Outline each Plasmodium parasite.
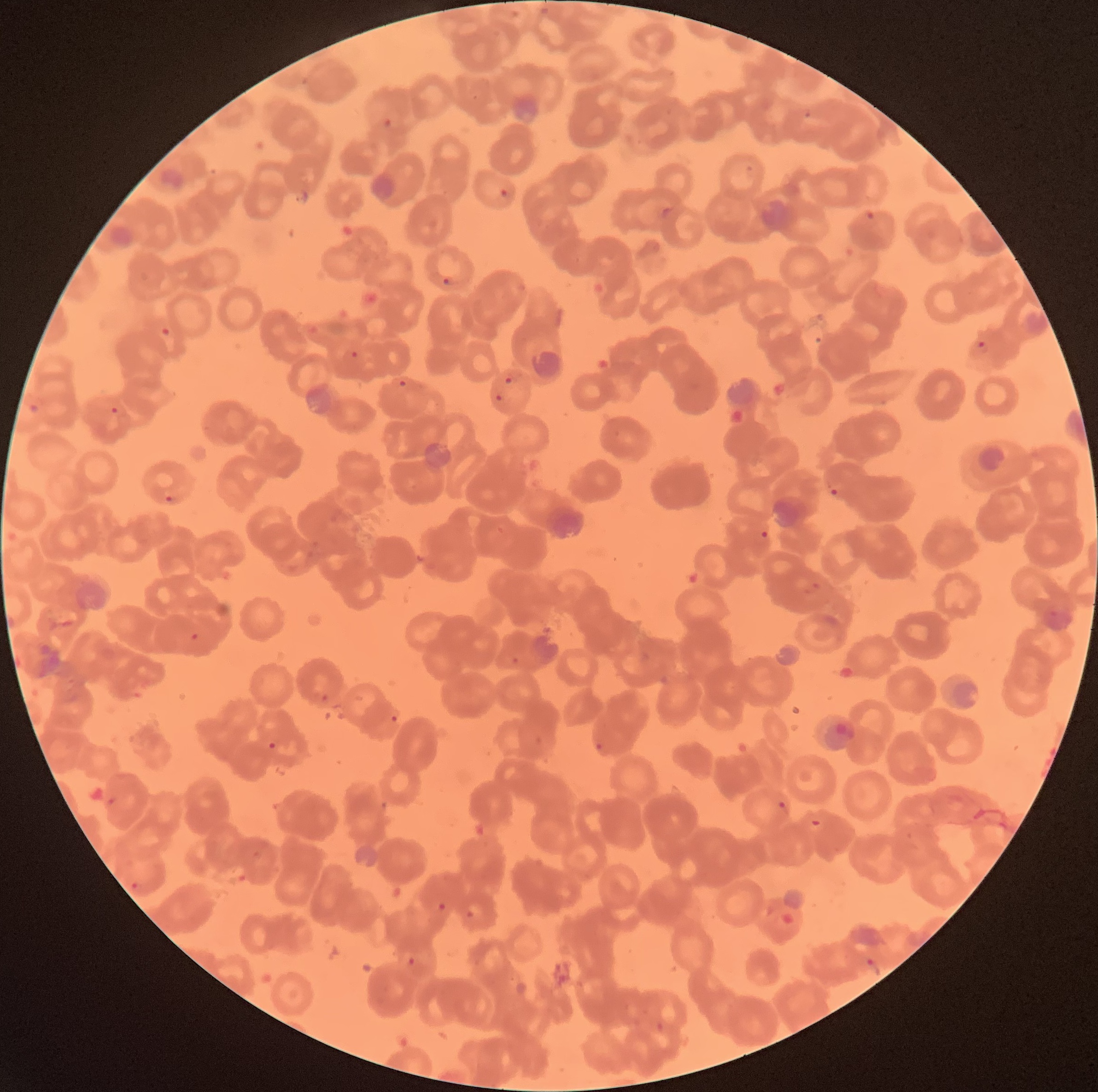
Approximate bounding boxes as (x1, y1, x2, y2) in pixels.
Plasmodium parasites: (804, 107, 812, 119), (381, 116, 392, 128), (745, 163, 758, 172), (499, 187, 509, 198), (865, 210, 875, 224), (443, 276, 457, 286), (971, 340, 990, 353), (351, 349, 359, 359), (503, 372, 524, 385), (398, 379, 408, 387), (494, 394, 511, 410), (109, 405, 120, 414), (829, 483, 845, 496), (162, 493, 176, 503), (759, 530, 770, 539), (803, 583, 821, 595), (511, 656, 519, 664), (389, 714, 399, 724), (267, 740, 277, 750), (595, 742, 604, 750), (777, 800, 786, 810), (807, 819, 821, 828), (129, 879, 141, 893), (437, 902, 447, 912), (406, 955, 417, 967), (863, 957, 877, 968).

{
  "preparation": "thin blood smear",
  "image_size": "1098×1092 pixels",
  "modality": "optical microscopy",
  "red_blood_cell_morphology": "rouleaux formation"
}